Report the malaria status of this cell.
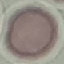

Uninfected.

Giemsa-stained preparation. Acquired by smartphone through the microscope eyepiece. Thin blood smear. Automatically extracted cell patch, resized to 64 × 64 pixels.